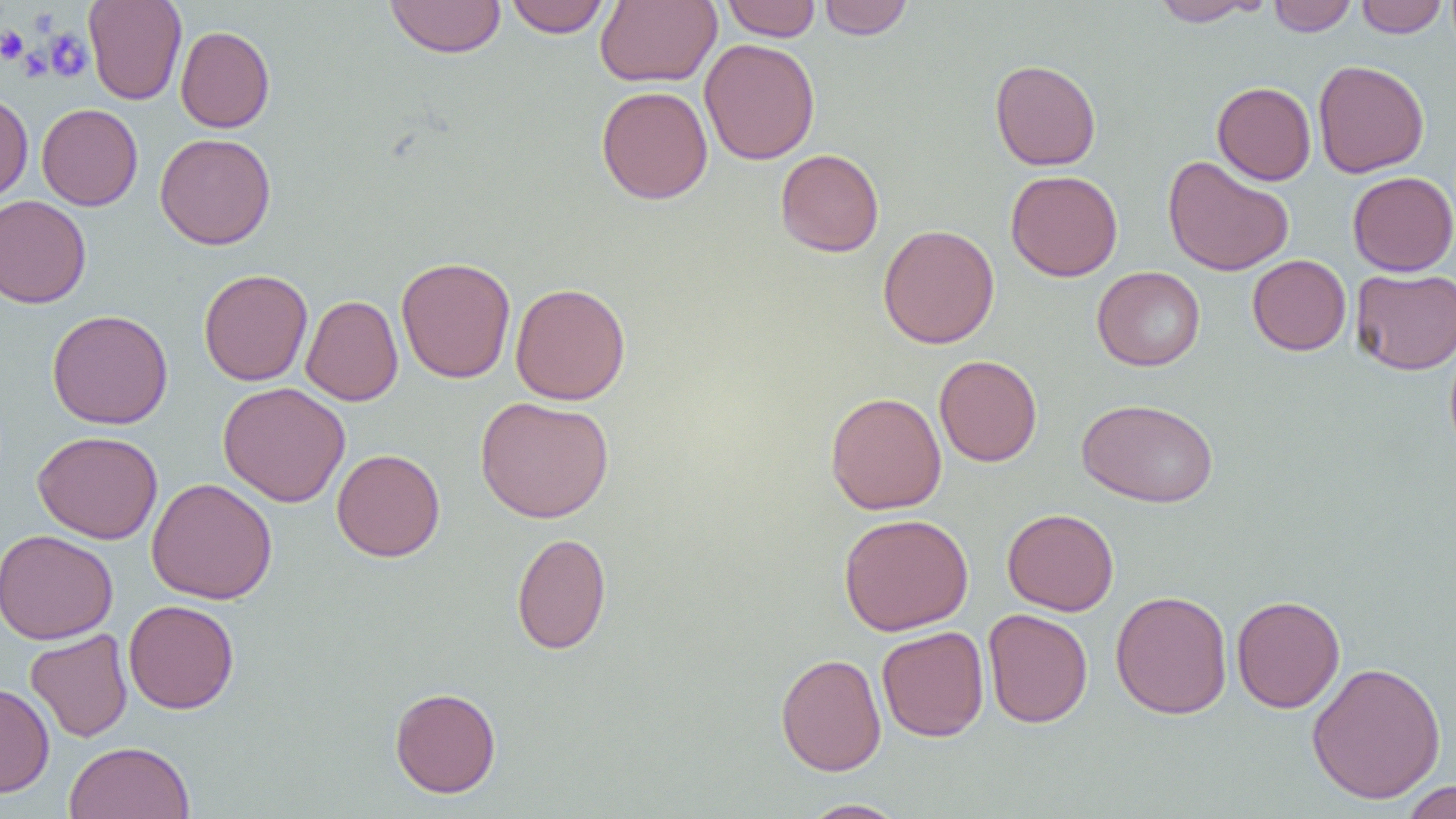
Approximate bounding boxes as (x1,y1)-(x2,y2) corner pairs in pixels. Platelet locations: (0,25)-(29,64), (45,29)-(92,82), (18,47)-(51,81). Uninfected red blood cell locations: (83,0)-(187,105), (384,0)-(506,58), (505,0)-(610,38), (595,0)-(721,87), (721,0)-(821,41), (818,0)-(914,40), (1150,0)-(1264,26), (1268,0)-(1357,35), (1355,0)-(1448,37), (175,25)-(275,133), (699,38)-(820,165), (989,59)-(1101,171), (1313,59)-(1430,178), (1212,81)-(1316,185), (596,85)-(713,204), (0,91)-(33,203), (37,103)-(143,211), (155,133)-(276,249), (775,148)-(884,257), (1162,155)-(1294,276), (1006,170)-(1123,281), (1348,171)-(1456,276), (0,195)-(91,308), (877,224)-(1000,349), (1247,254)-(1351,355), (396,256)-(516,383), (1092,266)-(1206,371), (198,268)-(313,386), (1351,268)-(1456,374), (510,282)-(631,405), (301,295)-(403,406), (47,309)-(173,430), (1445,336)-(1456,461), (934,354)-(1042,466), (218,381)-(350,507), (825,391)-(947,515), (475,396)-(614,523), (1077,397)-(1219,508), (32,430)-(163,544), (331,449)-(445,562), (146,477)-(278,604), (1002,508)-(1119,616), (838,513)-(974,636), (0,529)-(117,645), (511,532)-(612,655), (1111,590)-(1233,719), (1231,594)-(1345,713), (123,599)-(239,714), (982,608)-(1093,728), (876,625)-(989,742), (25,629)-(133,742), (775,653)-(887,776), (1306,661)-(1447,805), (0,682)-(55,797), (389,687)-(502,798), (63,741)-(195,818), (1401,780)-(1456,819), (799,799)-(908,818). Slide-level diagnosis: negative for blood parasites. Image is 1456×819 pixels. Thin blood smear. Captured at 1000x magnification. One field of a larger specimen. Optical microscopy.